Assess this cell for malaria.
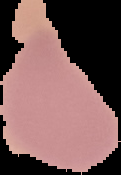

Uninfected.

From a thin blood smear. The area outside the segmented cell region is set to black. Image is 121×175 pixels.